Give a bounding box for every malaria parasite, every leukocyte, and every artifact (stain precipitate or debris).
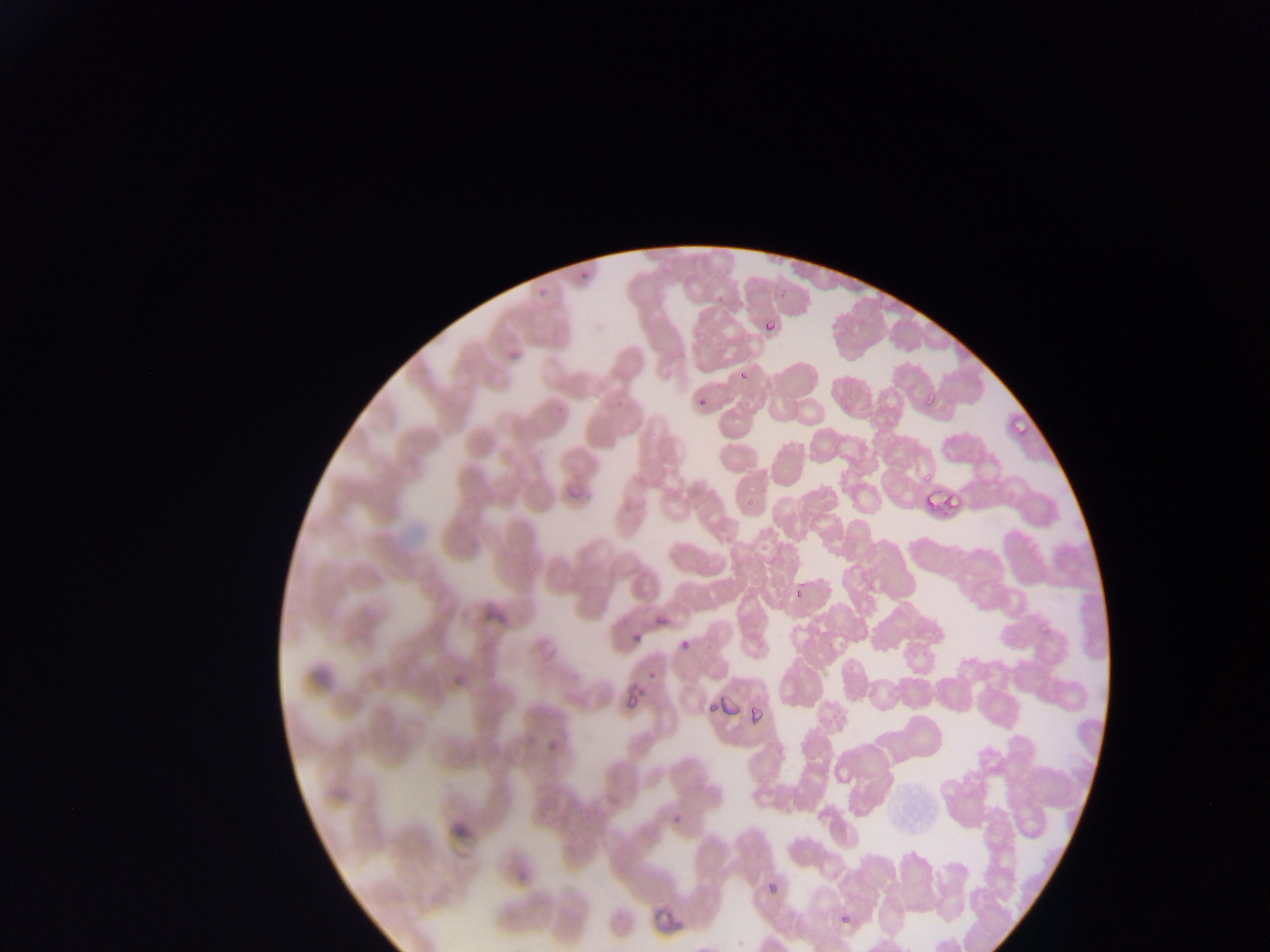
Approximate bounding boxes as {left, top, right, bottom} in pixels.
Malaria parasites (some below the resolvable threshold): {576, 267, 593, 282}, {534, 289, 551, 300}, {761, 315, 784, 337}, {503, 344, 522, 362}, {736, 371, 753, 384}, {695, 395, 706, 407}, {563, 480, 591, 510}, {922, 487, 959, 510}, {790, 583, 807, 605}, {653, 602, 673, 630}, {630, 624, 648, 643}, {680, 630, 703, 645}, {675, 642, 691, 657}, {645, 667, 660, 677}, {623, 681, 644, 716}, {720, 699, 740, 719}, {698, 703, 715, 717}, {747, 704, 763, 723}, {544, 735, 560, 755}, {671, 801, 694, 826}, {759, 878, 783, 901}, {647, 900, 688, 933}.
No leukocytes observed.

country = Ghana
capture = mobile-phone photograph through a microscope
preparation = thin blood film
image size = 1270×952 pixels
field of view = single